Locate every blood parasite and identify its species.
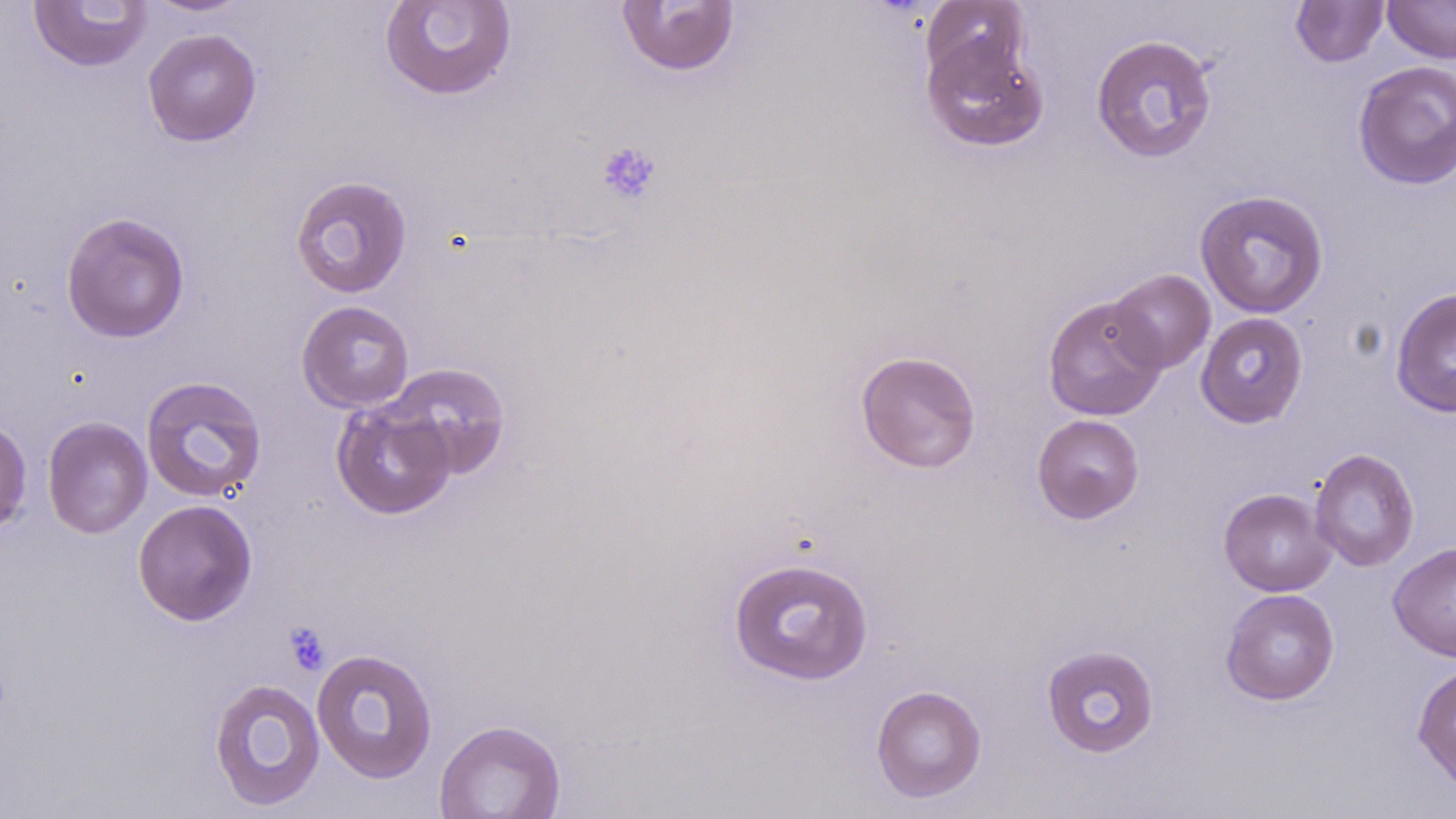

No blood parasites observed.

Summary:
  - Coordinate format: approximate bounding boxes as (x1, y1, x2, y2) in pixels
  - Platelet locations: (596, 140, 662, 206), (283, 621, 331, 675)
  - Uninfected red blood cell locations: (142, 0, 253, 17), (379, 0, 517, 101), (615, 0, 741, 77), (1290, 0, 1389, 67), (1382, 0, 1456, 63), (28, 1, 153, 73), (921, 1, 1030, 89), (142, 28, 262, 146), (1090, 33, 1218, 164), (922, 34, 1048, 153), (1353, 60, 1456, 190), (289, 175, 413, 298), (1194, 189, 1329, 318), (60, 210, 190, 343), (1107, 268, 1216, 374), (1390, 287, 1456, 417), (1042, 295, 1167, 421), (296, 300, 415, 412), (1195, 312, 1308, 428), (855, 350, 982, 473), (383, 362, 512, 479), (140, 375, 268, 503), (332, 400, 457, 519), (1032, 414, 1145, 524), (42, 416, 153, 538), (0, 418, 32, 537), (1309, 448, 1420, 571), (1218, 488, 1337, 596), (132, 499, 258, 625), (1389, 541, 1456, 662), (728, 556, 874, 685), (1220, 588, 1340, 705), (1041, 643, 1160, 758), (311, 647, 438, 784), (1412, 662, 1456, 794), (208, 677, 326, 811), (871, 684, 986, 803), (434, 718, 566, 818)
  - Slide-level diagnosis: no evidence of blood parasites
  - Preparation: thin blood film
  - Field of view: single
  - Magnification: 1000x
  - Stain: May-Grünwald-Giemsa
  - Image size: 1456×819 pixels
  - Modality: optical microscopy